Point out each Plasmodium parasite.
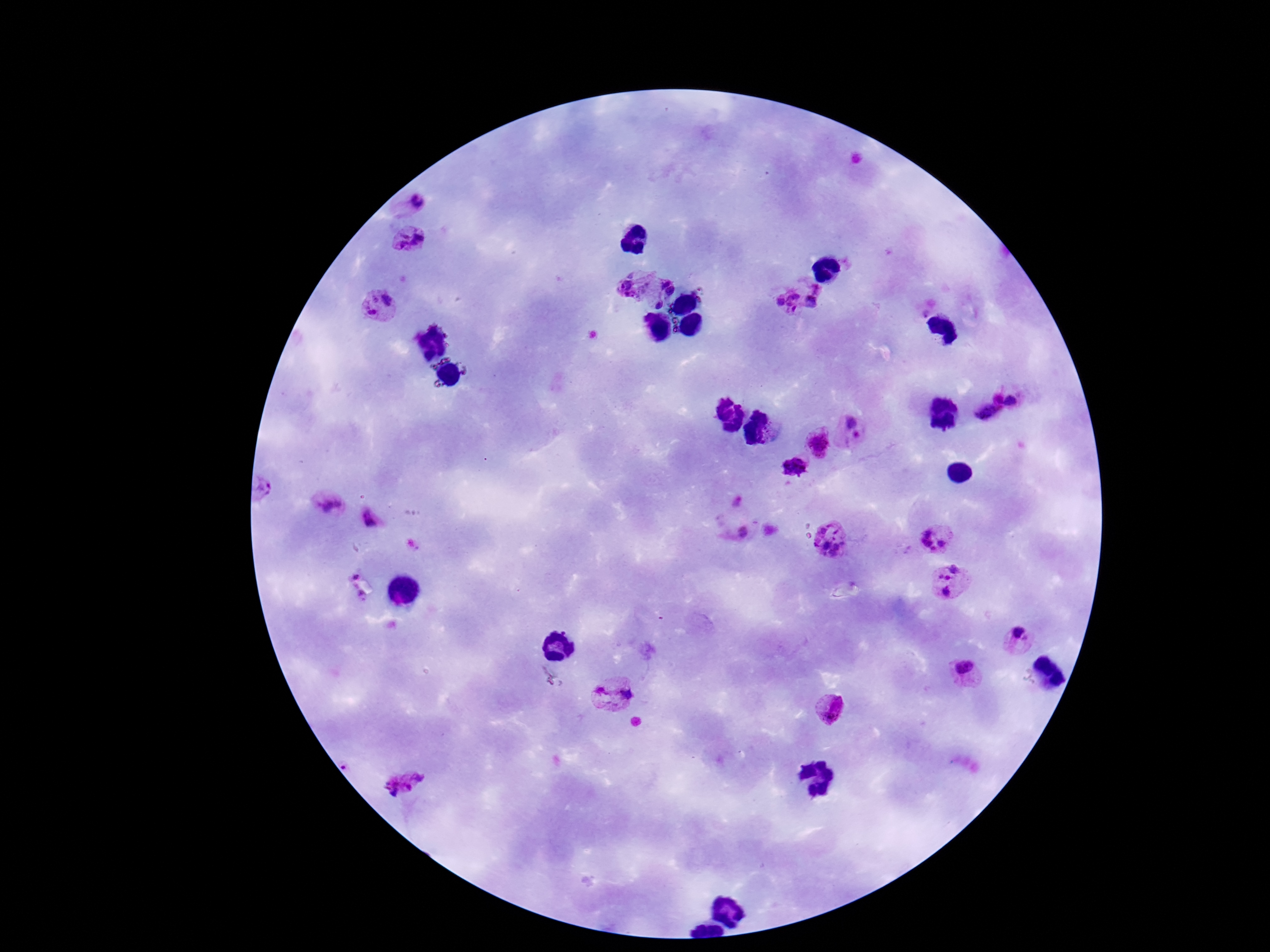
Approximate centers as [x, y] in pixels.
Plasmodium parasites: [416, 204], [410, 237], [630, 284], [669, 287], [386, 298], [789, 300], [817, 302], [660, 304], [369, 309], [926, 313], [997, 397], [1014, 400], [987, 416], [775, 429], [857, 430], [816, 443], [794, 472], [262, 489], [738, 502], [328, 506], [371, 518], [741, 532], [936, 536], [831, 540], [953, 579], [1020, 639], [966, 672], [612, 691], [832, 708], [403, 784].

Summary:
  - Preparation: thick blood smear
  - Capture: smartphone camera through the microscope eyepiece
  - Stain: Giemsa
  - Magnification: 100x
  - Field of view: one from this slide
  - Patient malaria status: positive
  - Image size: 1270×952 pixels